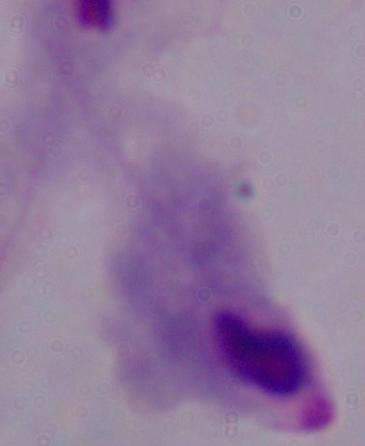
Summary:
  - Identification: trichomonad
  - Modality: micrograph
  - Magnification: 1000x